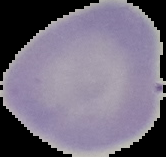

Summary:
  - Image size: 166×157 pixels
  - Malaria status: uninfected
  - Preparation: thin blood film
  - Image type: segmented cell region with the area outside set to black